Outline each Plasmodium malariae-infected red blood cell.
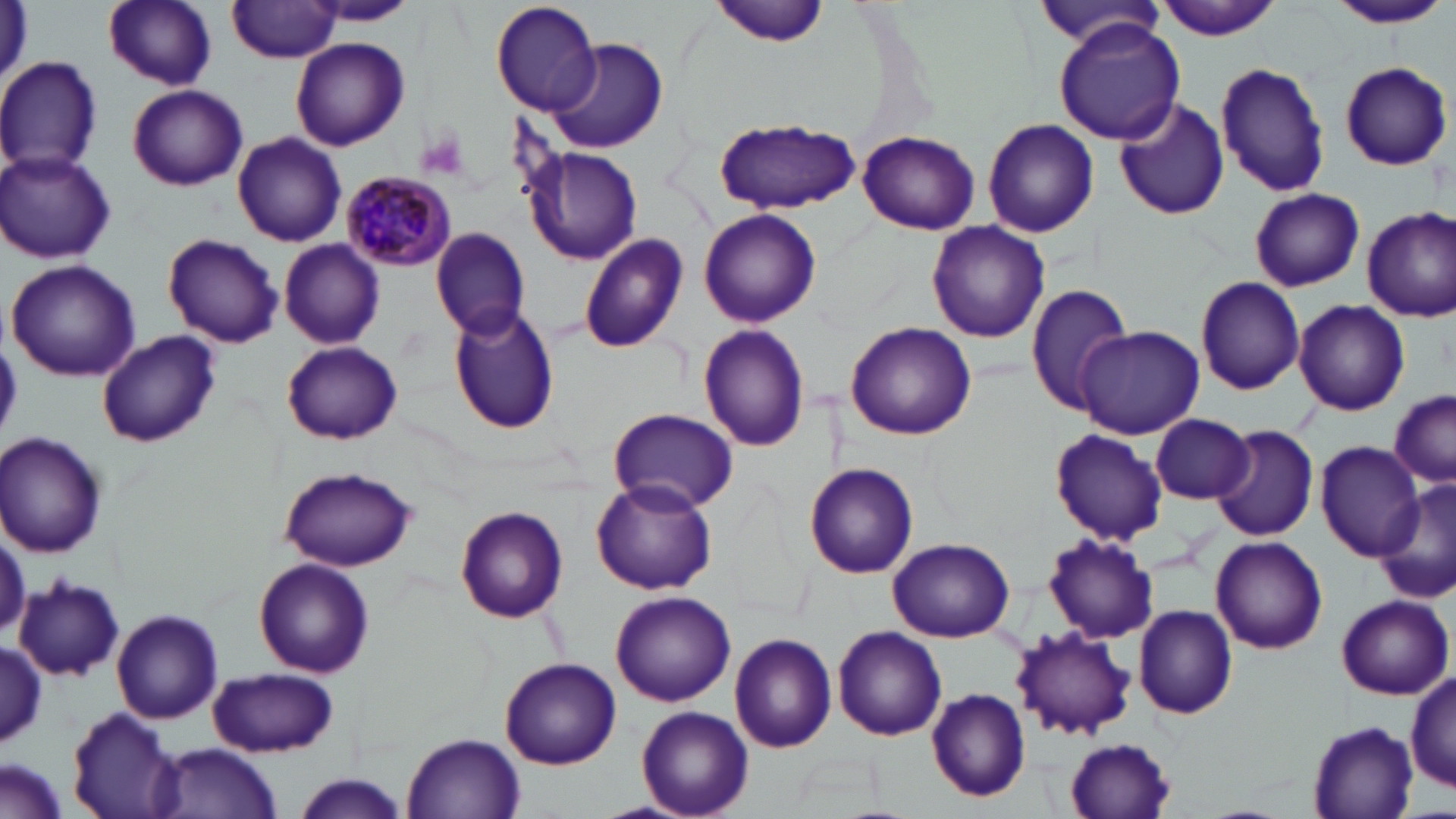
Approximate bounding boxes as named x1/y1/x2/y2 corners in pixels.
Plasmodium malariae-infected red blood cells: (x1=340, y1=174, x2=455, y2=268).

Summary:
  - Platelet locations: (x1=419, y1=132, x2=467, y2=182)
  - Uninfected red blood cell locations: (x1=103, y1=0, x2=219, y2=90), (x1=491, y1=0, x2=600, y2=116), (x1=710, y1=0, x2=836, y2=46), (x1=1153, y1=0, x2=1282, y2=41), (x1=1325, y1=0, x2=1453, y2=29), (x1=228, y1=1, x2=342, y2=62), (x1=304, y1=1, x2=417, y2=25), (x1=1033, y1=4, x2=1167, y2=54), (x1=1054, y1=20, x2=1184, y2=146), (x1=291, y1=37, x2=410, y2=151), (x1=547, y1=37, x2=666, y2=153), (x1=0, y1=57, x2=101, y2=175), (x1=1216, y1=59, x2=1328, y2=196), (x1=1338, y1=61, x2=1451, y2=170), (x1=127, y1=85, x2=247, y2=190), (x1=1113, y1=96, x2=1230, y2=220), (x1=711, y1=117, x2=862, y2=212), (x1=982, y1=118, x2=1100, y2=239), (x1=858, y1=130, x2=979, y2=235), (x1=232, y1=132, x2=346, y2=247), (x1=527, y1=147, x2=641, y2=263), (x1=0, y1=151, x2=116, y2=265), (x1=1249, y1=187, x2=1366, y2=293), (x1=1362, y1=207, x2=1456, y2=321), (x1=699, y1=208, x2=821, y2=328), (x1=927, y1=220, x2=1051, y2=343), (x1=430, y1=228, x2=530, y2=341), (x1=163, y1=233, x2=284, y2=349), (x1=577, y1=234, x2=689, y2=355), (x1=279, y1=239, x2=385, y2=348), (x1=6, y1=259, x2=141, y2=382), (x1=1194, y1=277, x2=1305, y2=395), (x1=1024, y1=283, x2=1135, y2=415), (x1=1293, y1=300, x2=1411, y2=417), (x1=448, y1=306, x2=560, y2=434), (x1=844, y1=321, x2=976, y2=439), (x1=699, y1=323, x2=810, y2=451), (x1=1074, y1=325, x2=1204, y2=439), (x1=95, y1=329, x2=219, y2=445), (x1=282, y1=341, x2=402, y2=444), (x1=1388, y1=388, x2=1455, y2=485), (x1=609, y1=407, x2=737, y2=512), (x1=1150, y1=412, x2=1254, y2=504), (x1=1211, y1=424, x2=1320, y2=542), (x1=1049, y1=428, x2=1169, y2=545), (x1=1, y1=432, x2=107, y2=555), (x1=1316, y1=442, x2=1425, y2=561), (x1=807, y1=464, x2=918, y2=579), (x1=278, y1=466, x2=419, y2=573), (x1=591, y1=479, x2=718, y2=596), (x1=1376, y1=482, x2=1456, y2=604), (x1=456, y1=504, x2=569, y2=623), (x1=0, y1=530, x2=26, y2=636), (x1=1042, y1=534, x2=1159, y2=644), (x1=1211, y1=535, x2=1328, y2=654), (x1=888, y1=537, x2=1017, y2=640), (x1=255, y1=558, x2=374, y2=676), (x1=14, y1=576, x2=125, y2=682), (x1=612, y1=591, x2=735, y2=706), (x1=1335, y1=594, x2=1453, y2=700), (x1=1134, y1=605, x2=1239, y2=720), (x1=113, y1=610, x2=223, y2=724), (x1=833, y1=626, x2=947, y2=741), (x1=1011, y1=627, x2=1135, y2=740), (x1=730, y1=633, x2=839, y2=753), (x1=0, y1=642, x2=46, y2=751), (x1=499, y1=657, x2=620, y2=768), (x1=208, y1=668, x2=340, y2=757), (x1=1408, y1=669, x2=1455, y2=792), (x1=924, y1=686, x2=1031, y2=804), (x1=66, y1=702, x2=185, y2=816), (x1=637, y1=706, x2=754, y2=818), (x1=1306, y1=721, x2=1422, y2=818), (x1=400, y1=733, x2=527, y2=818), (x1=1065, y1=737, x2=1178, y2=819), (x1=152, y1=743, x2=285, y2=818), (x1=2, y1=759, x2=69, y2=819), (x1=287, y1=776, x2=413, y2=817)
  - Slide-level diagnosis: Plasmodium malariae
  - Magnification: 1000x
  - Field of view: single
  - Stain: May-Grünwald-Giemsa
  - Image size: 1456×819 pixels
  - Preparation: thin blood smear
  - Modality: optical microscopy